Locate every blood parasite and identify its species.
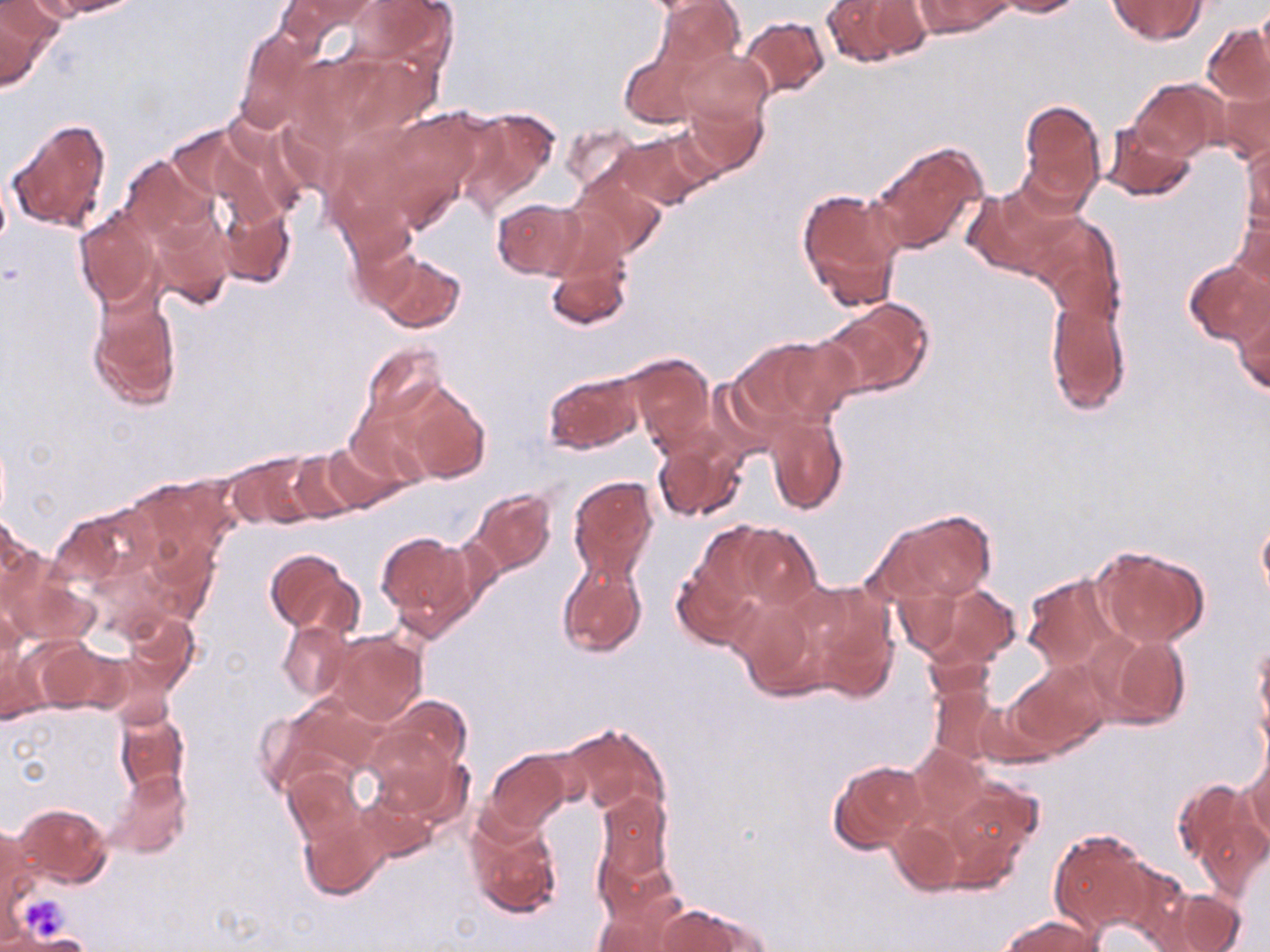
No blood parasites seen.

Approximate bounding boxes as (x1,y1)-(x2,y2) corner pairs in pixels. Platelet locations: (22,895)-(73,940). Uninfected red blood cell locations: (43,0)-(139,18), (275,0)-(377,48), (343,0)-(458,69), (656,0)-(743,72), (822,0)-(927,68), (917,0)-(1008,38), (995,0)-(1085,16), (1105,0)-(1208,45), (1256,3)-(1270,80), (0,4)-(55,90), (739,16)-(830,99), (1203,25)-(1269,104), (233,28)-(321,133), (615,47)-(702,130), (673,49)-(772,131), (1213,66)-(1270,165), (1128,78)-(1225,161), (679,97)-(768,180), (1018,99)-(1106,210), (455,108)-(559,213), (6,117)-(114,236), (1101,122)-(1198,203), (561,123)-(641,193), (613,130)-(712,210), (1241,131)-(1270,229), (867,143)-(986,255), (119,154)-(214,242), (567,167)-(664,259), (964,183)-(1079,281), (797,187)-(905,312), (492,199)-(584,280), (218,203)-(297,291), (1229,205)-(1270,297), (149,208)-(236,310), (74,209)-(162,309), (1033,214)-(1126,318), (344,224)-(422,312), (374,253)-(466,332), (545,254)-(632,332), (1182,259)-(1270,346), (88,288)-(183,410), (1045,293)-(1132,413), (823,299)-(935,398), (1232,304)-(1270,397), (730,334)-(853,431), (357,342)-(451,431), (627,354)-(714,449), (543,372)-(641,454), (396,380)-(491,483), (765,412)-(848,514), (654,435)-(749,524), (319,439)-(410,515), (288,450)-(366,521), (227,453)-(319,529), (125,475)-(237,566), (569,475)-(660,580), (470,489)-(556,574), (56,504)-(158,590), (876,508)-(995,606), (1257,513)-(1270,606), (2,514)-(40,611), (732,523)-(822,613), (376,531)-(478,634), (1091,545)-(1209,647), (264,548)-(360,639), (671,558)-(759,650), (556,560)-(647,659), (1021,573)-(1122,672), (9,575)-(97,646), (794,580)-(899,700), (924,583)-(1018,667), (731,593)-(828,700), (1,605)-(23,685), (122,613)-(198,690), (277,621)-(353,701), (1087,628)-(1192,732), (325,632)-(427,726), (32,639)-(117,716), (0,642)-(44,724), (922,644)-(996,704), (1255,645)-(1270,743), (1005,661)-(1110,756), (928,686)-(1005,767), (280,694)-(387,780), (372,696)-(471,795), (112,708)-(189,799), (560,722)-(669,818), (367,733)-(470,829), (908,745)-(986,827), (1242,748)-(1270,848), (484,750)-(572,834), (828,760)-(927,854), (107,768)-(191,859), (283,768)-(366,849), (938,779)-(1039,881), (1171,780)-(1266,897), (351,789)-(439,866), (594,790)-(673,888), (12,802)-(113,889), (466,809)-(563,919), (298,813)-(386,901), (888,816)-(967,897), (1,821)-(40,933), (1048,828)-(1153,934), (1160,889)-(1252,952), (592,896)-(688,952), (654,903)-(768,952), (998,914)-(1101,952). Slide-level diagnosis: no evidence of blood parasites. May-Grünwald-Giemsa-stained preparation. Optical microscopy. Captured at 1000x magnification. Thin blood film. Image is 1270×952 pixels. Single field of view.